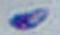
Summary:
  - Modality: photomicrograph
  - Identification: Toxoplasma gondii
  - Magnification: 1000x